Report the malaria status of this cell.
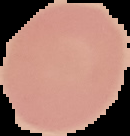
It is uninfected.

Summary:
  - Image size: 130×136 pixels
  - Preparation: thin blood smear
  - Image type: segmented cell region on a black background